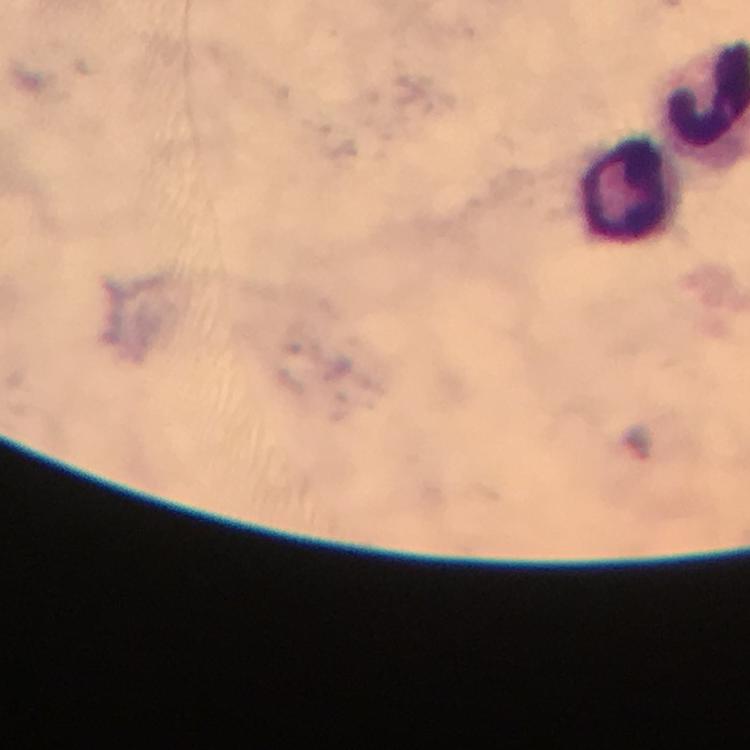

{
  "stain": "Giemsa",
  "immersion_oil": "applied",
  "image_size": "750×750 pixels",
  "preparation": "thick blood smear",
  "malaria_parasites": "none detected",
  "capture": "smartphone camera through the microscope",
  "cropped_from": "a single field of view",
  "magnification": "100x",
  "leukocyte_locations": "approximate object centers, in pixels from the top-left corner: (x=633, y=187)",
  "context": "from a diagnostic examination for malaria"
}